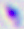

Summary:
  - Identification: Toxoplasma gondii
  - Modality: micrograph
  - Magnification: 400x